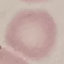
Malaria status: uninfected. Acquired by smartphone through the microscope eyepiece. Automatically extracted cell patch, resized to 64 × 64 pixels. Giemsa stain. Thin blood smear.